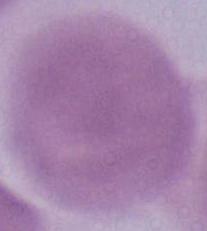

An erythrocyte is shown. Captured at 1000x magnification. Photomicrograph.